Locate every leukocyte (white blood cell).
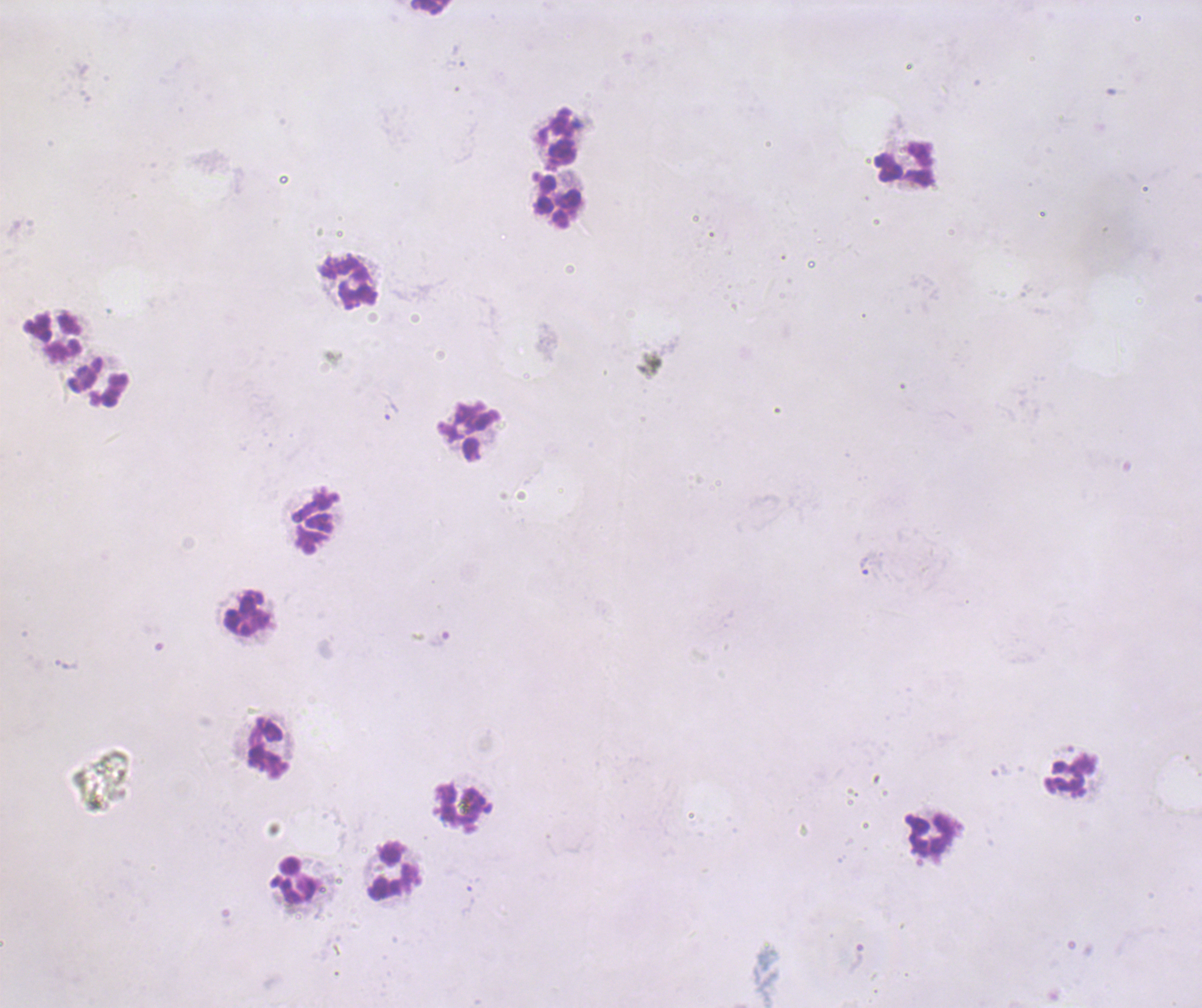
Approximate object centers, in pixels from the top-left corner.
Leukocytes: (x=430, y=7), (x=556, y=139), (x=905, y=164), (x=558, y=202), (x=349, y=282), (x=53, y=337), (x=98, y=383), (x=469, y=431), (x=246, y=613), (x=268, y=748), (x=1070, y=776), (x=460, y=807), (x=928, y=835), (x=393, y=870), (x=295, y=881).

Approximate object centers, in pixels from the top-left corner.
Summary:
  - Trophozoite locations: (x=391, y=411), (x=864, y=565)
  - Magnification: 100x
  - Field of view: single
  - Result: positive for Plasmodium parasites
  - Background quality: unsatisfactory
  - Preparation: thick smear of blood
  - Context: previously used in an actual diagnosis
  - Stain: Romanowsky
  - Image size: 1202×1008 pixels
  - Coloration quality: bad